Give a bounding box for every Plasmodium parasite.
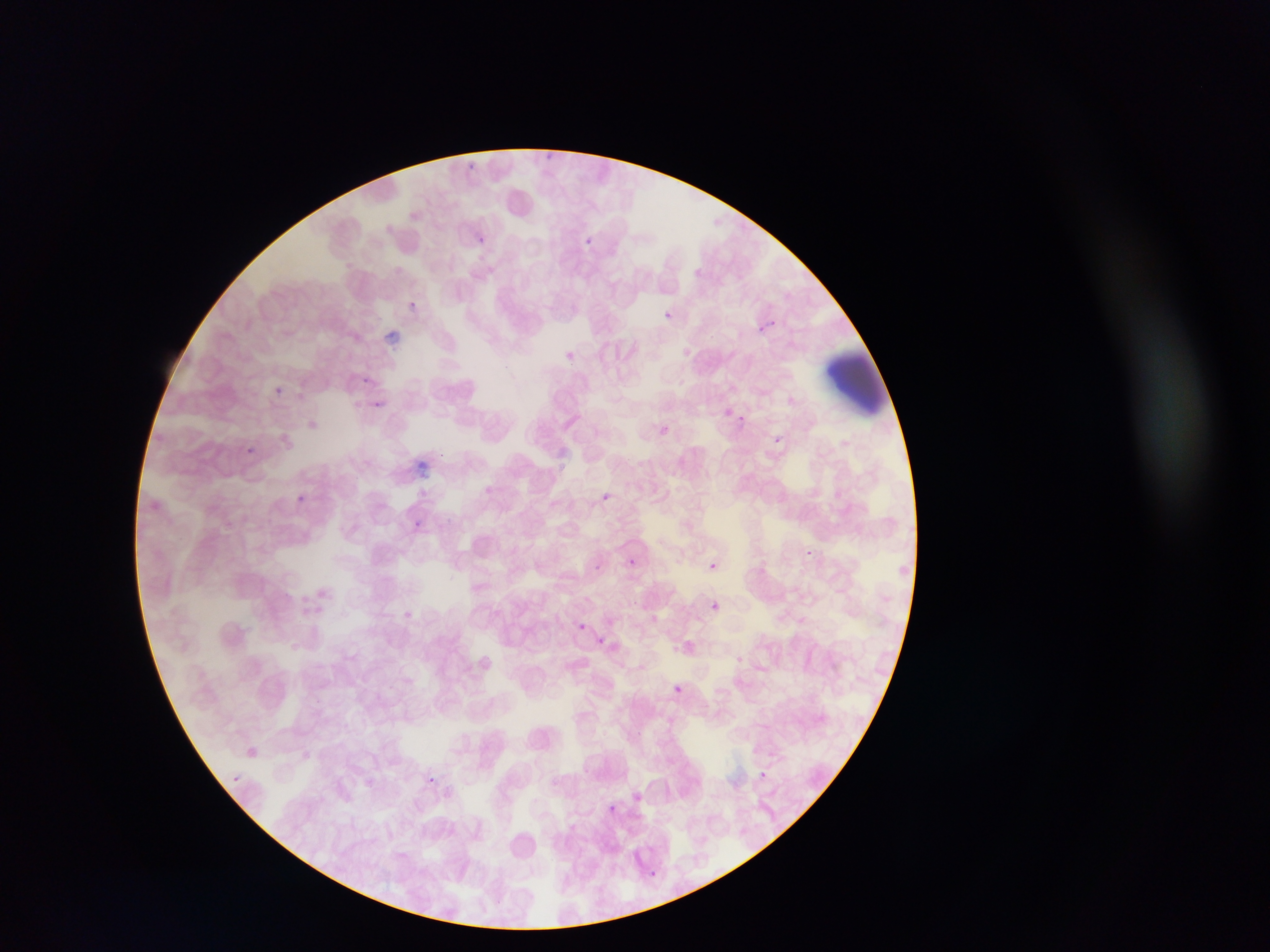
Approximate bounding boxes as left top right bottom in pixels.
Plasmodium parasites: 545 149 559 162; 463 160 478 170; 582 234 596 247; 475 236 486 245; 409 297 421 314; 665 307 672 316; 753 318 775 337; 564 350 576 361; 359 373 371 389; 274 388 288 399; 371 399 385 412; 721 407 732 417; 737 414 746 423; 654 424 670 439; 772 436 782 445; 242 444 257 458; 600 492 612 503; 296 494 310 503; 412 518 423 531; 807 547 815 556; 628 558 637 567; 706 560 719 571; 594 561 602 572; 708 599 723 613; 573 619 589 634; 593 636 609 650; 672 685 683 695; 234 736 262 784; 240 742 262 763; 226 773 243 789; 428 774 437 782; 650 868 658 877 | approximate x y pixel centers of objects too small to bound: 763 772; 612 807.

capture: mobile-phone photograph through a microscope
image_size: 1270×952 pixels
preparation: thin blood smear
artifact_stain_precipitate_or_debris_locations: 'approximate bounding boxes as left top right bottom in pixels: 381 328 407 348; 827 350 890 415; 413 458 428 484'
country: Ghana
field_of_view: single